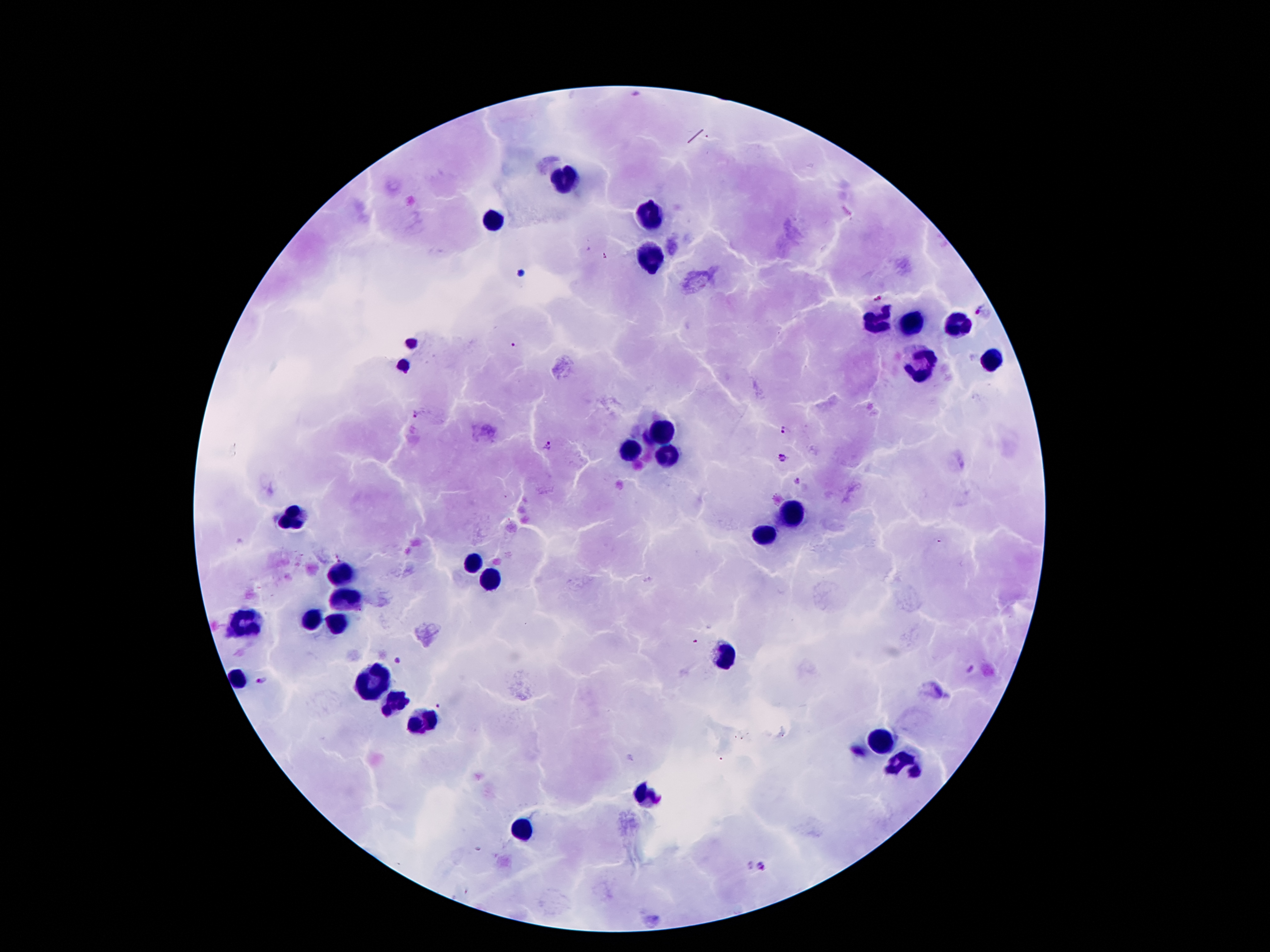

leukocyte_locations: 'approximate centers as [x, y] in pixels: [567, 178], [649, 221], [496, 223], [651, 257], [875, 322], [910, 322], [957, 324], [992, 361], [920, 369], [658, 434], [630, 451], [666, 451], [791, 512], [291, 518], [765, 533], [472, 561], [345, 570], [492, 578], [348, 602], [311, 621], [240, 624], [337, 624], [727, 662], [236, 678], [373, 682], [391, 701], [421, 723], [882, 742], [907, 764], [647, 794], [524, 830]'
preparation: thick blood smear
patient_malaria_status: positive for Plasmodium falciparum
image_size: 1270×952 pixels
capture: smartphone camera through the microscope eyepiece
field_of_view: one from this slide
magnification: 100x
plasmodium_parasite_locations: 'approximate centers as [x, y] in pixels: [417, 415], [785, 430], [545, 447], [783, 458], [796, 479], [400, 663], [970, 667], [261, 679], [762, 865]'
stain: Giemsa